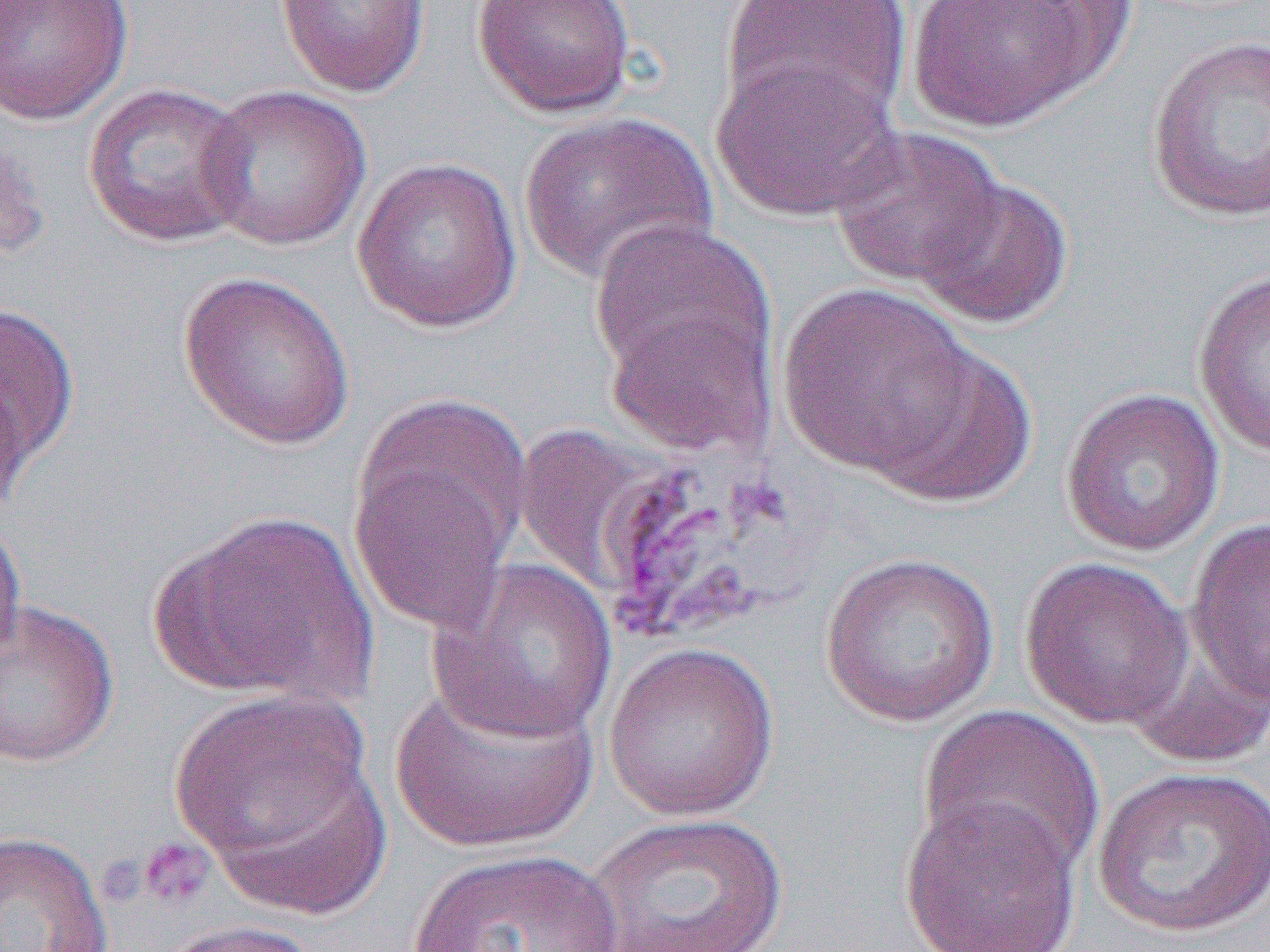
Summary:
  - Coordinate format: approximate bounding boxes as (x1,y1)-(x2,y2) corner pairs in pixels
  - Platelet locations: (135,837)-(216,912)
  - Uninfected red blood cell locations: (275,0)-(431,98), (471,0)-(638,118), (904,0)-(1121,132), (0,1)-(135,125), (719,1)-(912,131), (1145,33)-(1270,223), (711,54)-(902,223), (81,82)-(253,248), (194,83)-(371,251), (518,110)-(717,288), (828,125)-(1006,289), (0,135)-(50,271), (351,157)-(523,334), (913,175)-(1074,329), (588,219)-(775,398), (177,269)-(356,451), (1192,269)-(1270,457), (776,282)-(981,478), (1,301)-(80,496), (863,338)-(1038,509), (1060,388)-(1225,557), (348,425)-(526,639), (151,510)-(378,707), (0,514)-(27,672), (1185,516)-(1270,710), (819,552)-(1001,727), (427,557)-(618,744), (1018,557)-(1194,729), (0,598)-(119,768), (1120,633)-(1270,769), (602,641)-(779,821), (388,672)-(599,853), (169,691)-(380,884), (915,705)-(1105,881), (1092,764)-(1270,939), (898,792)-(1085,952), (581,811)-(791,952), (0,829)-(114,952), (405,848)-(632,952), (151,918)-(322,952)
  - Slide-level diagnosis: Plasmodium vivax
  - Preparation: thin blood film
  - Magnification: 1000x
  - Field of view: one of a larger specimen
  - Modality: light microscopy
  - Image size: 1270×952 pixels